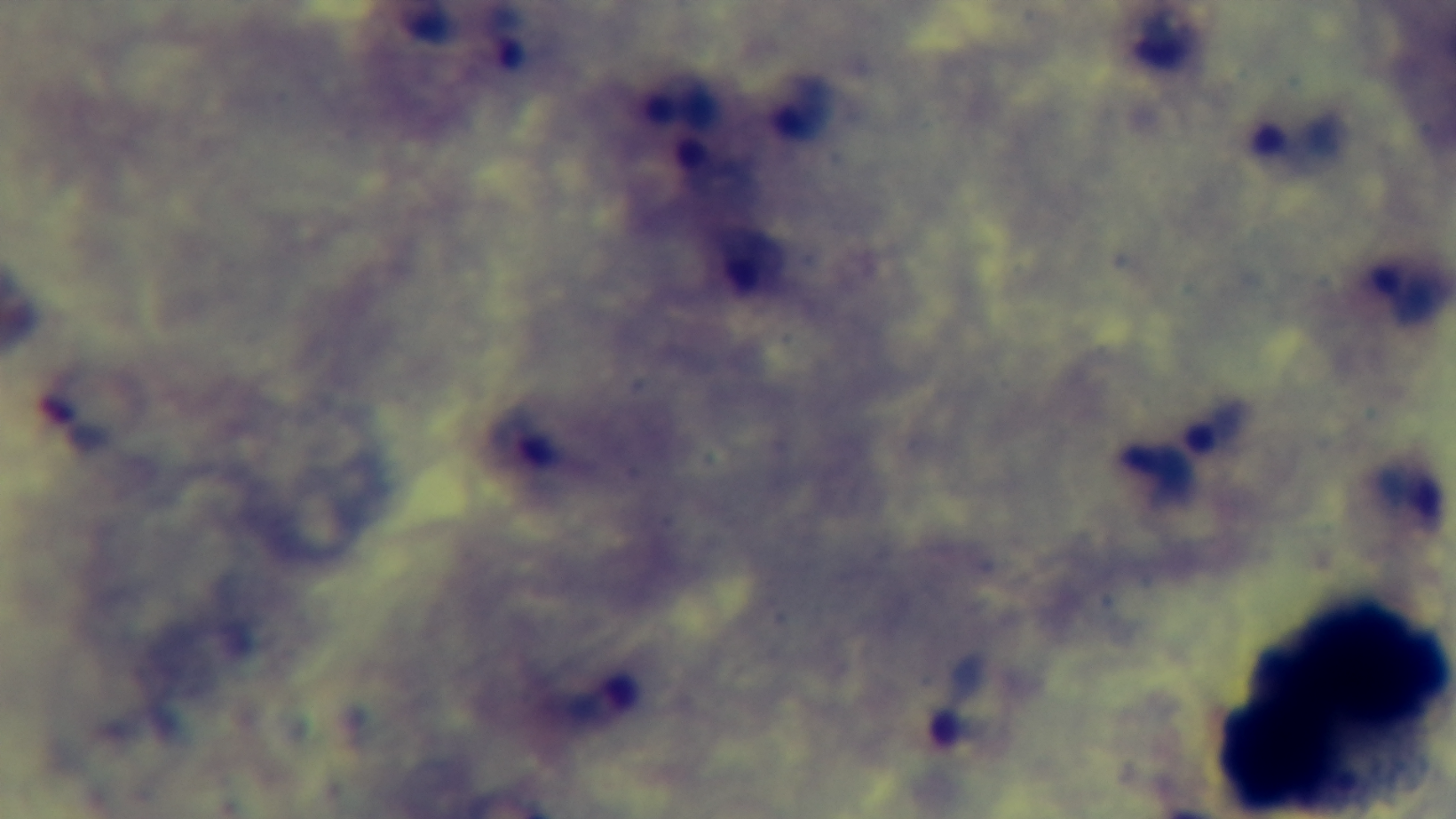
modality = light microscopy
stain = Giemsa
field of view = one from the slide
preparation = thick
capture = mounted 4K digital camera
malaria status = positive
objective = 100x oil immersion